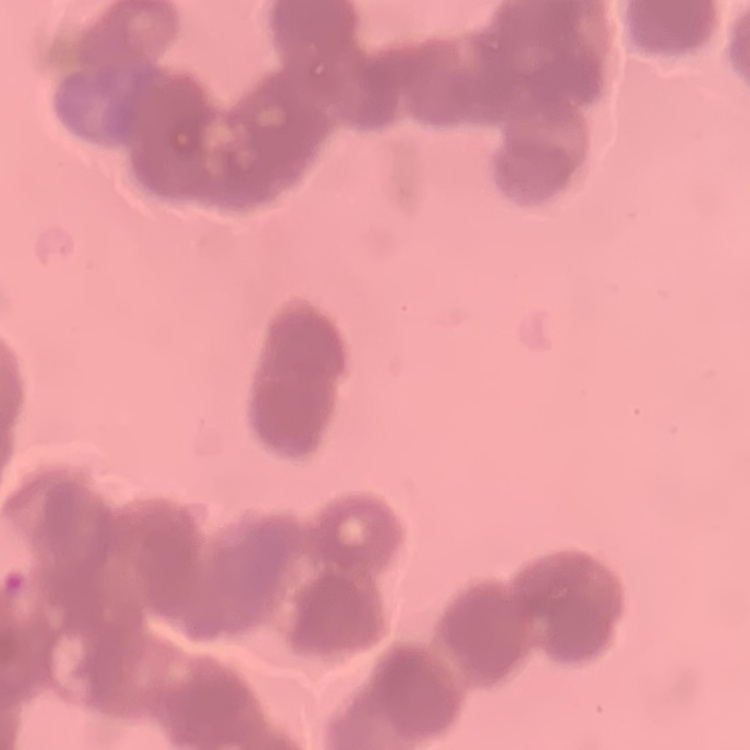
erythrocyte morphology = rouleaux formation
stain = Field's or Giemsa
preparation = thin peripheral smear
image type = square crop of a larger photomicrograph